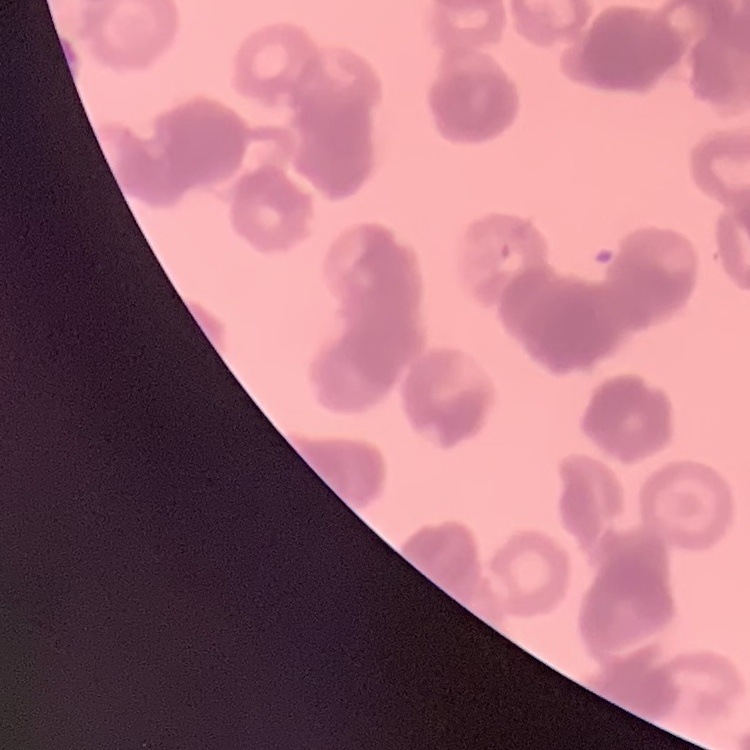
red blood cell morphology = rouleaux formation
preparation = thin blood smear
stain = Field's or Giemsa
image type = one tile cut from a larger photomicrograph